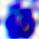

Summary:
  - Modality: micrograph
  - Identification: white blood cell
  - Magnification: 400x